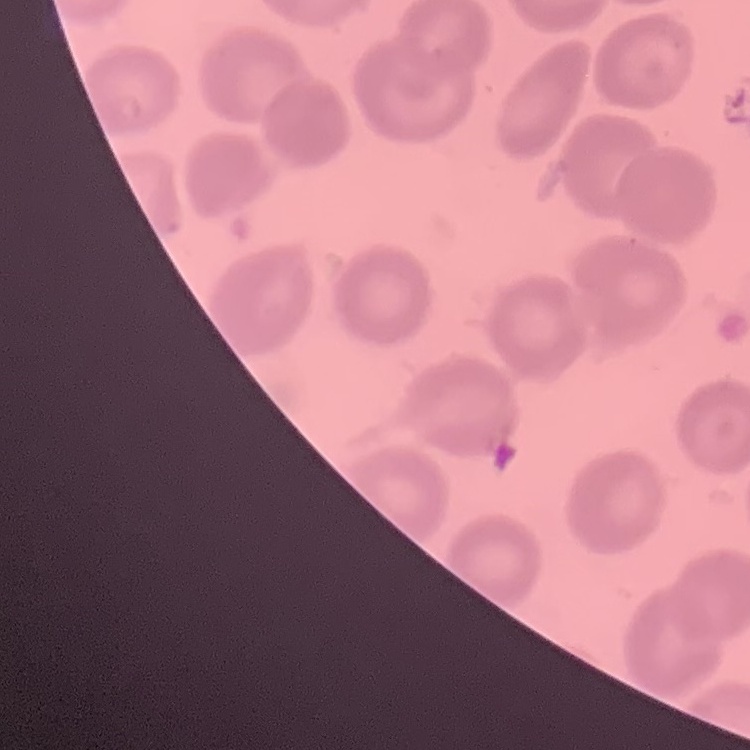

Summary:
  - Erythrocyte morphology: no rouleaux formation
  - Image type: square crop of a larger photomicrograph
  - Stain: Field's or Giemsa
  - Preparation: thin peripheral smear